Describe the morphology of the erythrocytes.
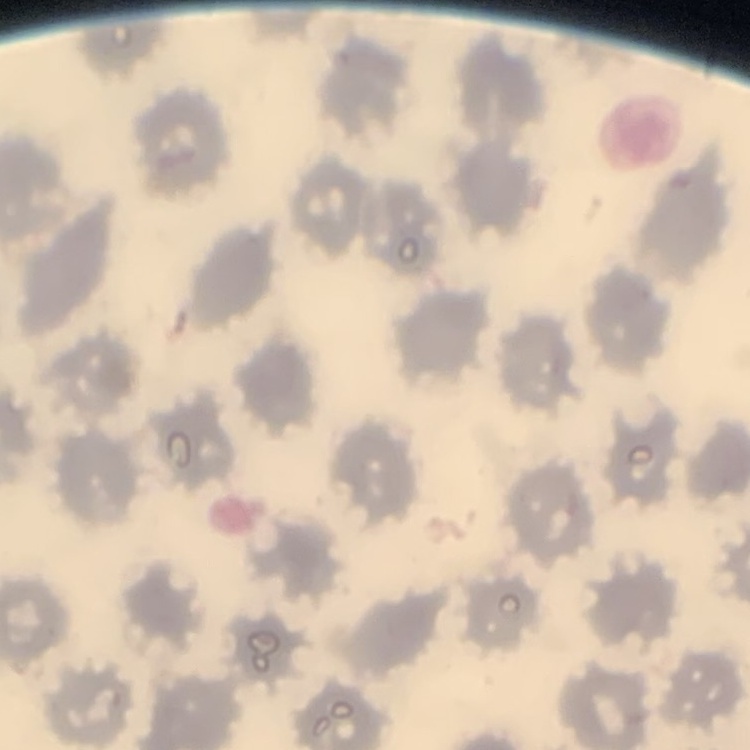

No rouleaux formation.

Summary:
  - Preparation: thin blood film
  - Image type: square crop of a larger photomicrograph
  - Stain: Field's or Giemsa